Describe the morphology of the erythrocytes.
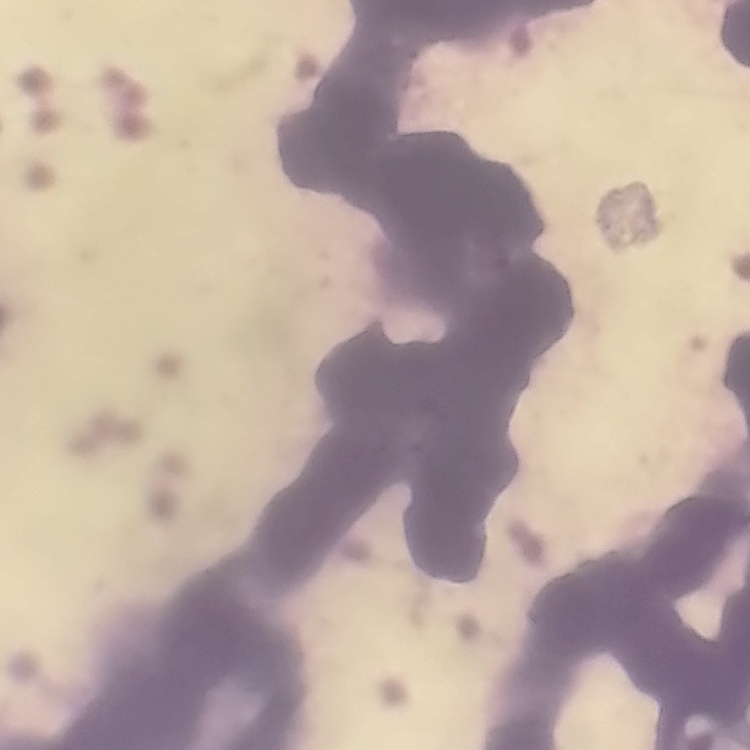
Rouleaux formation.

Stained with either Field's or Giemsa. One tile cut from a larger photomicrograph. Thin blood smear.